Give the position of every malaria parasite and every leukocyte.
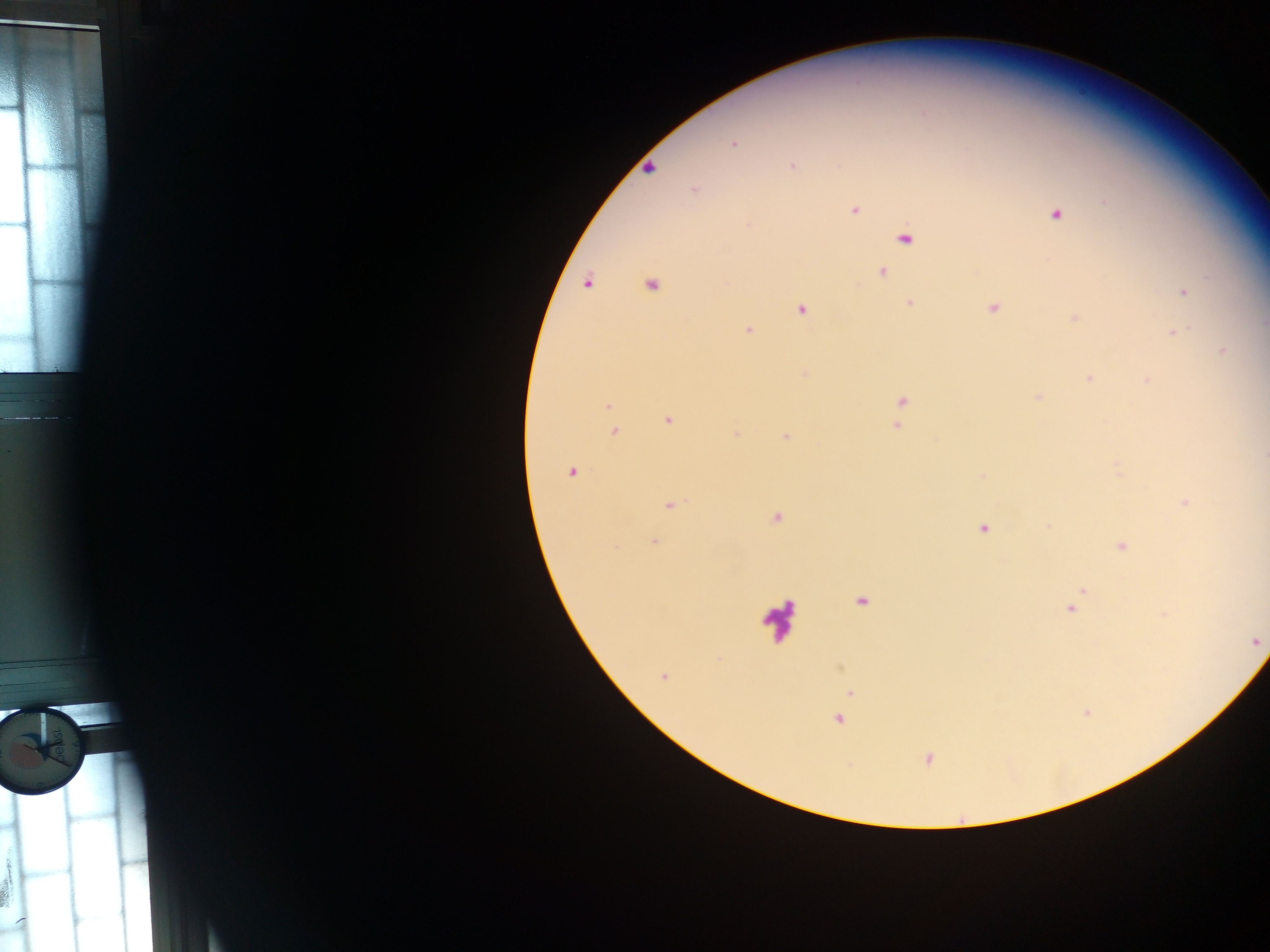

Approximate centers as {x, y} in pixels.
Malaria parasites: {733, 143}, {792, 166}, {650, 168}, {694, 191}, {854, 210}, {1056, 215}, {748, 225}, {905, 238}, {883, 273}, {587, 283}, {651, 285}, {1184, 293}, {910, 302}, {993, 308}, {801, 310}, {1074, 318}, {748, 330}, {1173, 333}, {1223, 351}, {804, 373}, {1089, 378}, {1147, 380}, {1038, 397}, {901, 401}, {607, 405}, {668, 420}, {897, 426}, {615, 432}, {736, 434}, {786, 436}, {1264, 455}, {571, 473}, {982, 476}, {1184, 503}, {671, 505}, {775, 519}, {1049, 526}, {983, 529}, {654, 541}, {1122, 546}, {1081, 591}, {861, 601}, {1071, 607}, {1256, 642}, {663, 676}, {851, 692}, {838, 719}, {929, 758}, {19, 922}.
Leukocytes: {777, 618}.

Photographed through a microscope with a mobile-phone camera. Image is 1270×952 pixels. Single field of view. Thick blood film. Sample from Ghana.